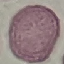

Summary:
  - Result: no malaria parasites detected
  - Stain: Giemsa
  - Capture: smartphone camera at the microscope eyepiece
  - Preparation: thin blood smear
  - Image type: cell patch, automatically extracted from a larger field of view and resized to 64 × 64 pixels